Evaluate for malaria.
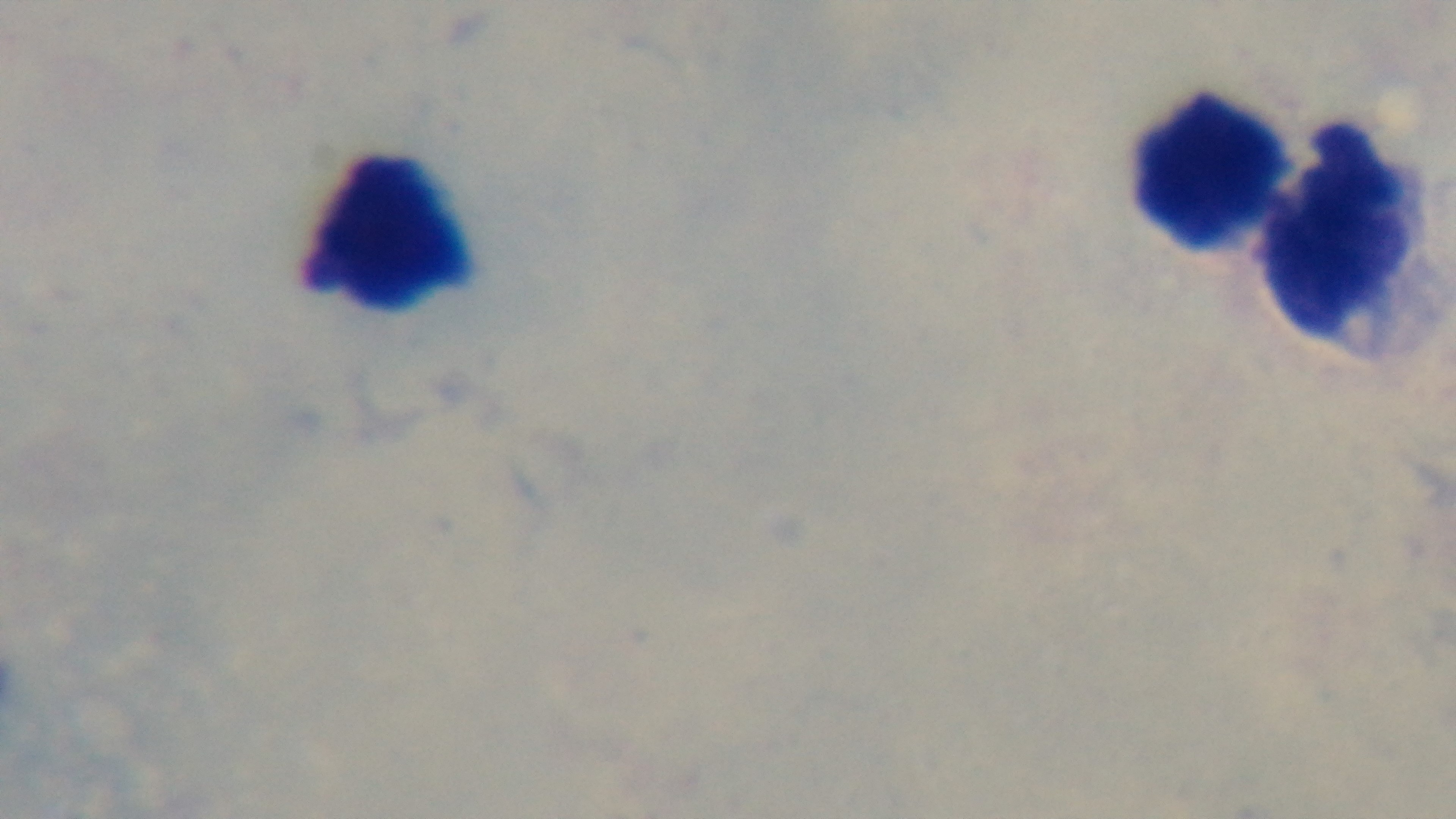

Uninfected.

preparation = thick blood film
stain = Giemsa
objective = 100x oil immersion
field of view = one from the slide
modality = light microscopy
capture = mounted 4K digital camera